Name the parasite shown.
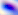

This is Toxoplasma gondii.

Photomicrograph. 400x magnification.